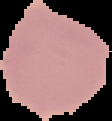

malaria status = uninfected
image size = 112×121 pixels
image type = segmented cell region on a black background
preparation = thin blood smear